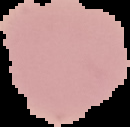

The area outside the segmented cell region is set to black. Malaria status: uninfected. From a thin blood smear. Image is 130×127 pixels.